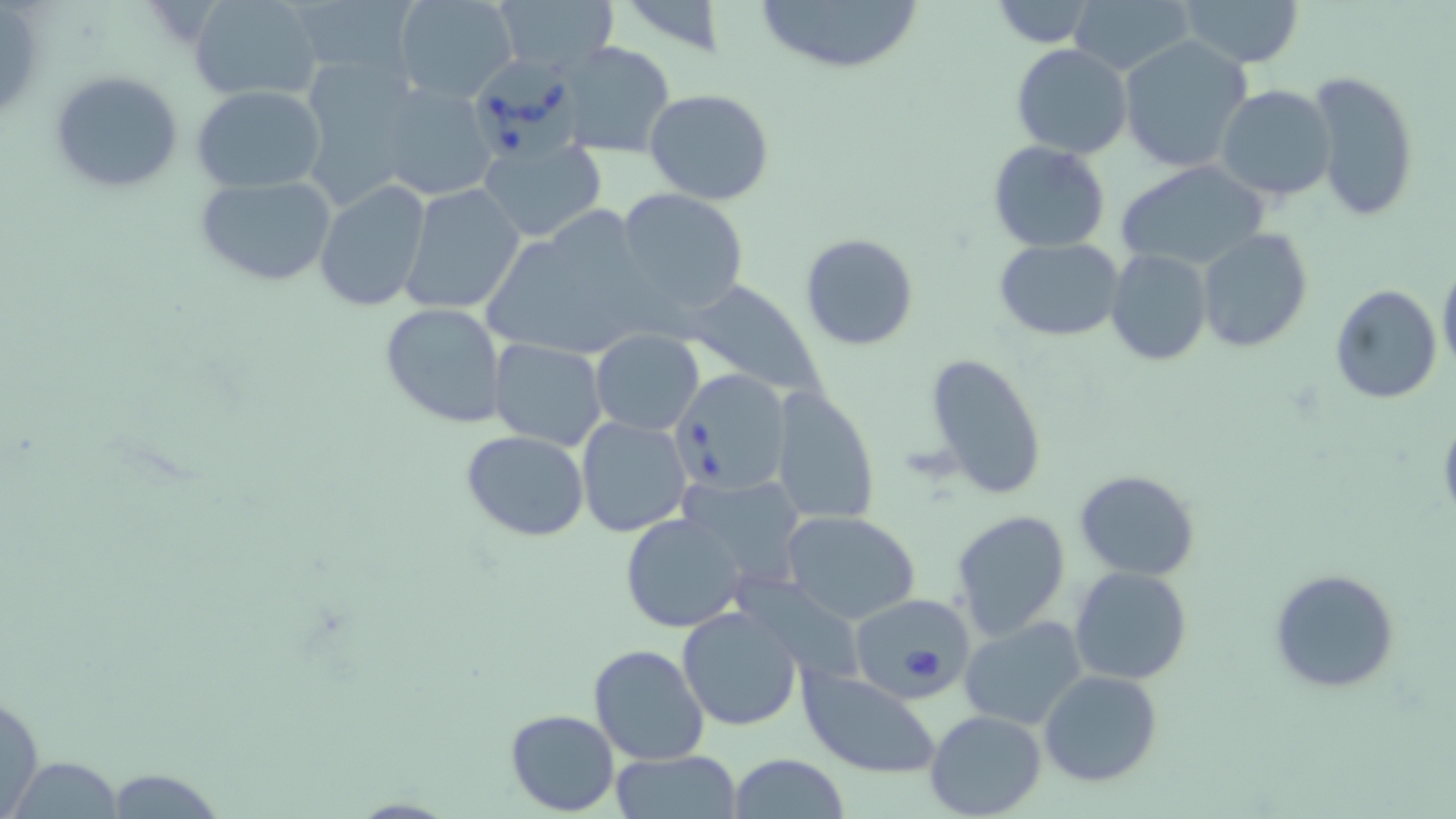
Summary:
  - Coordinate format: approximate bounding boxes as [x1, y1, x2, y2] in pixels
  - Babesia divergens-infected red blood cell locations: [470, 52, 584, 161], [672, 367, 791, 496], [849, 594, 972, 700]
  - Uninfected red blood cell locations: [189, 0, 326, 102], [286, 0, 424, 83], [393, 0, 519, 101], [749, 0, 928, 72], [1068, 0, 1196, 77], [1177, 0, 1303, 68], [490, 1, 620, 77], [985, 1, 1104, 48], [1118, 35, 1256, 174], [560, 41, 676, 158], [1011, 43, 1133, 160], [47, 68, 185, 194], [1307, 71, 1419, 224], [360, 80, 506, 205], [192, 85, 327, 192], [1216, 85, 1335, 200], [645, 89, 775, 205], [477, 137, 606, 241], [987, 142, 1111, 252], [1116, 160, 1270, 270], [193, 174, 338, 288], [313, 179, 432, 310], [399, 185, 525, 314], [614, 190, 749, 322], [480, 207, 667, 367], [1197, 229, 1314, 353], [798, 232, 921, 352], [994, 237, 1126, 342], [1105, 249, 1213, 366], [1437, 260, 1456, 378], [684, 280, 825, 400], [1330, 284, 1442, 404], [379, 303, 509, 428], [590, 330, 703, 435], [489, 338, 608, 451], [924, 353, 1049, 501], [769, 386, 880, 526], [575, 416, 693, 537], [462, 430, 590, 542], [1073, 468, 1202, 582], [678, 472, 809, 588], [950, 508, 1071, 641], [781, 511, 921, 625], [621, 513, 748, 631], [1069, 565, 1194, 685], [1269, 568, 1400, 694], [677, 605, 804, 732], [958, 615, 1090, 731], [987, 634, 1154, 764], [587, 644, 711, 767], [797, 667, 943, 779], [1039, 669, 1163, 787], [0, 685, 45, 819], [504, 709, 619, 816], [924, 710, 1046, 819], [611, 751, 742, 819], [12, 754, 121, 819], [728, 754, 850, 818], [115, 769, 222, 819]
  - Slide-level diagnosis: Babesia divergens
  - Modality: optical microscopy
  - Magnification: 1000x
  - Field of view: single
  - Image size: 1456×819 pixels
  - Preparation: thin blood film
  - Stain: May-Grünwald-Giemsa